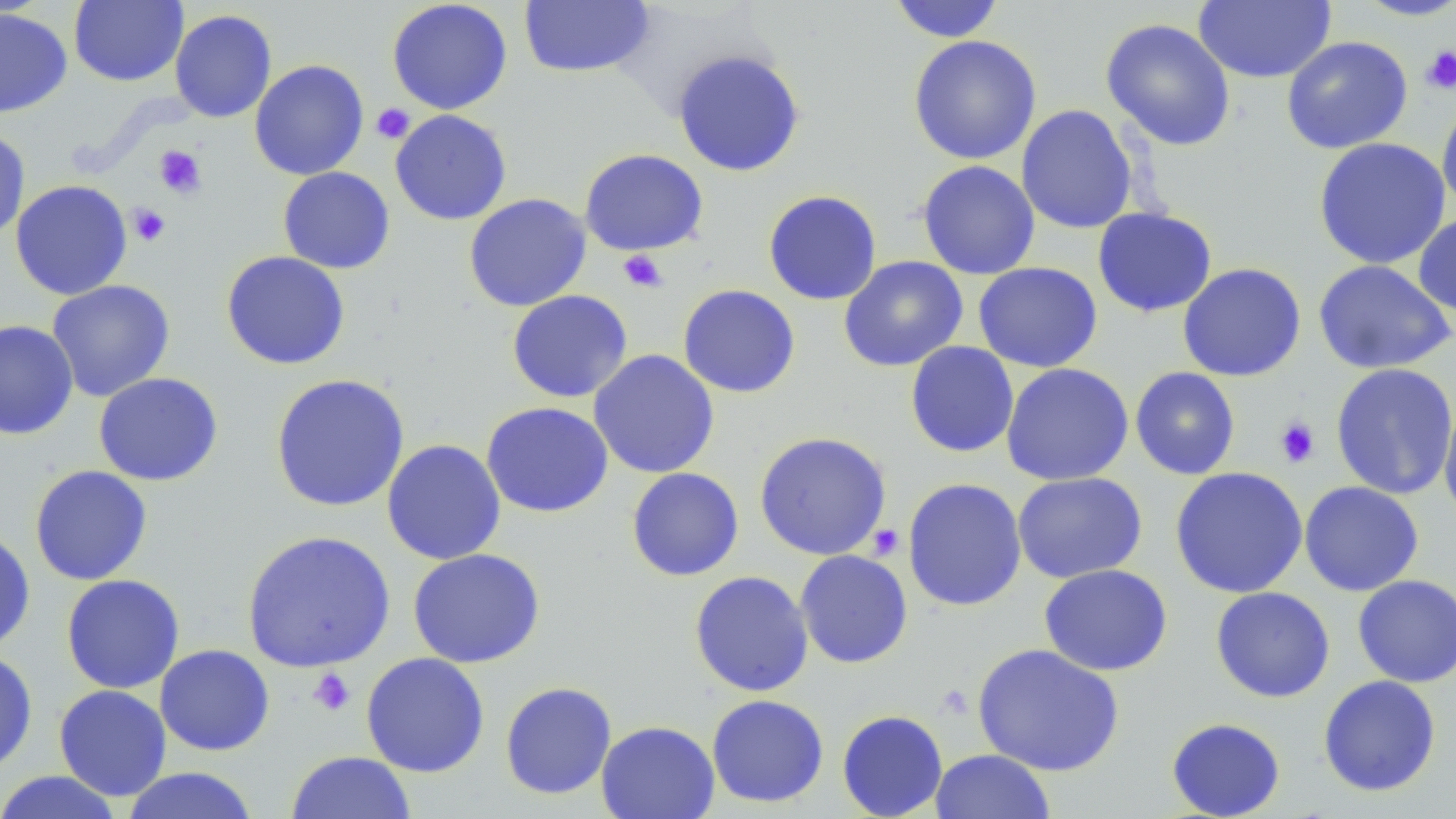

Summary:
  - Coordinate format: approximate bounding boxes as named x1/y1/x2/y2 corners in pixels
  - Platelet locations: (x1=1420, y1=45, x2=1456, y2=95), (x1=371, y1=103, x2=415, y2=144), (x1=154, y1=145, x2=207, y2=198), (x1=127, y1=203, x2=171, y2=246), (x1=618, y1=250, x2=668, y2=292), (x1=1274, y1=416, x2=1321, y2=468), (x1=867, y1=524, x2=904, y2=560), (x1=308, y1=668, x2=355, y2=716)
  - Uninfected red blood cell locations: (x1=69, y1=0, x2=188, y2=87), (x1=386, y1=0, x2=513, y2=115), (x1=887, y1=0, x2=1006, y2=43), (x1=1352, y1=0, x2=1456, y2=21), (x1=518, y1=1, x2=655, y2=78), (x1=1193, y1=1, x2=1336, y2=83), (x1=0, y1=8, x2=72, y2=118), (x1=169, y1=9, x2=277, y2=123), (x1=1100, y1=17, x2=1236, y2=151), (x1=907, y1=35, x2=1042, y2=165), (x1=1281, y1=36, x2=1413, y2=154), (x1=672, y1=48, x2=806, y2=177), (x1=249, y1=59, x2=369, y2=180), (x1=1436, y1=97, x2=1456, y2=216), (x1=1016, y1=104, x2=1138, y2=234), (x1=389, y1=109, x2=512, y2=225), (x1=0, y1=126, x2=31, y2=241), (x1=1313, y1=137, x2=1450, y2=269), (x1=578, y1=148, x2=709, y2=256), (x1=916, y1=160, x2=1041, y2=280), (x1=277, y1=167, x2=395, y2=274), (x1=10, y1=179, x2=133, y2=300), (x1=762, y1=190, x2=882, y2=306), (x1=463, y1=193, x2=592, y2=312), (x1=1092, y1=207, x2=1217, y2=317), (x1=1413, y1=212, x2=1456, y2=319), (x1=220, y1=250, x2=351, y2=370), (x1=838, y1=256, x2=968, y2=372), (x1=1312, y1=259, x2=1455, y2=375), (x1=973, y1=262, x2=1103, y2=373), (x1=1177, y1=262, x2=1307, y2=382), (x1=46, y1=279, x2=175, y2=402), (x1=677, y1=284, x2=801, y2=398), (x1=506, y1=289, x2=633, y2=403), (x1=0, y1=319, x2=79, y2=440), (x1=905, y1=341, x2=1019, y2=458), (x1=588, y1=349, x2=720, y2=479), (x1=1001, y1=363, x2=1134, y2=486), (x1=1330, y1=363, x2=1456, y2=500), (x1=1130, y1=367, x2=1241, y2=480), (x1=93, y1=372, x2=224, y2=486), (x1=269, y1=373, x2=410, y2=513), (x1=1438, y1=392, x2=1456, y2=528), (x1=480, y1=401, x2=614, y2=518), (x1=753, y1=431, x2=892, y2=561), (x1=381, y1=438, x2=506, y2=565), (x1=28, y1=464, x2=153, y2=586), (x1=1169, y1=466, x2=1308, y2=599), (x1=626, y1=467, x2=744, y2=582), (x1=1197, y1=467, x2=1323, y2=700), (x1=1012, y1=472, x2=1147, y2=583), (x1=901, y1=477, x2=1027, y2=611), (x1=1298, y1=481, x2=1424, y2=596), (x1=0, y1=527, x2=36, y2=655), (x1=241, y1=529, x2=396, y2=672), (x1=407, y1=547, x2=546, y2=668), (x1=794, y1=550, x2=913, y2=669), (x1=1038, y1=564, x2=1173, y2=676), (x1=689, y1=570, x2=814, y2=697), (x1=60, y1=574, x2=185, y2=694), (x1=1352, y1=574, x2=1456, y2=687), (x1=1210, y1=586, x2=1335, y2=703), (x1=971, y1=643, x2=1125, y2=776), (x1=154, y1=644, x2=275, y2=756), (x1=0, y1=648, x2=38, y2=776), (x1=360, y1=652, x2=490, y2=777), (x1=1318, y1=674, x2=1442, y2=797), (x1=499, y1=681, x2=617, y2=800), (x1=53, y1=684, x2=172, y2=801), (x1=706, y1=694, x2=829, y2=808), (x1=836, y1=709, x2=948, y2=819), (x1=1165, y1=717, x2=1286, y2=819), (x1=596, y1=720, x2=720, y2=819), (x1=929, y1=748, x2=1055, y2=819), (x1=285, y1=751, x2=416, y2=818), (x1=119, y1=767, x2=260, y2=819), (x1=0, y1=770, x2=126, y2=819)
  - Slide-level diagnosis: negative for blood parasites
  - Image size: 1456×819 pixels
  - Preparation: thin blood film
  - Modality: light microscopy
  - Magnification: 1000x
  - Stain: May-Grünwald-Giemsa
  - Field of view: one of a larger specimen